Classify the preparation.
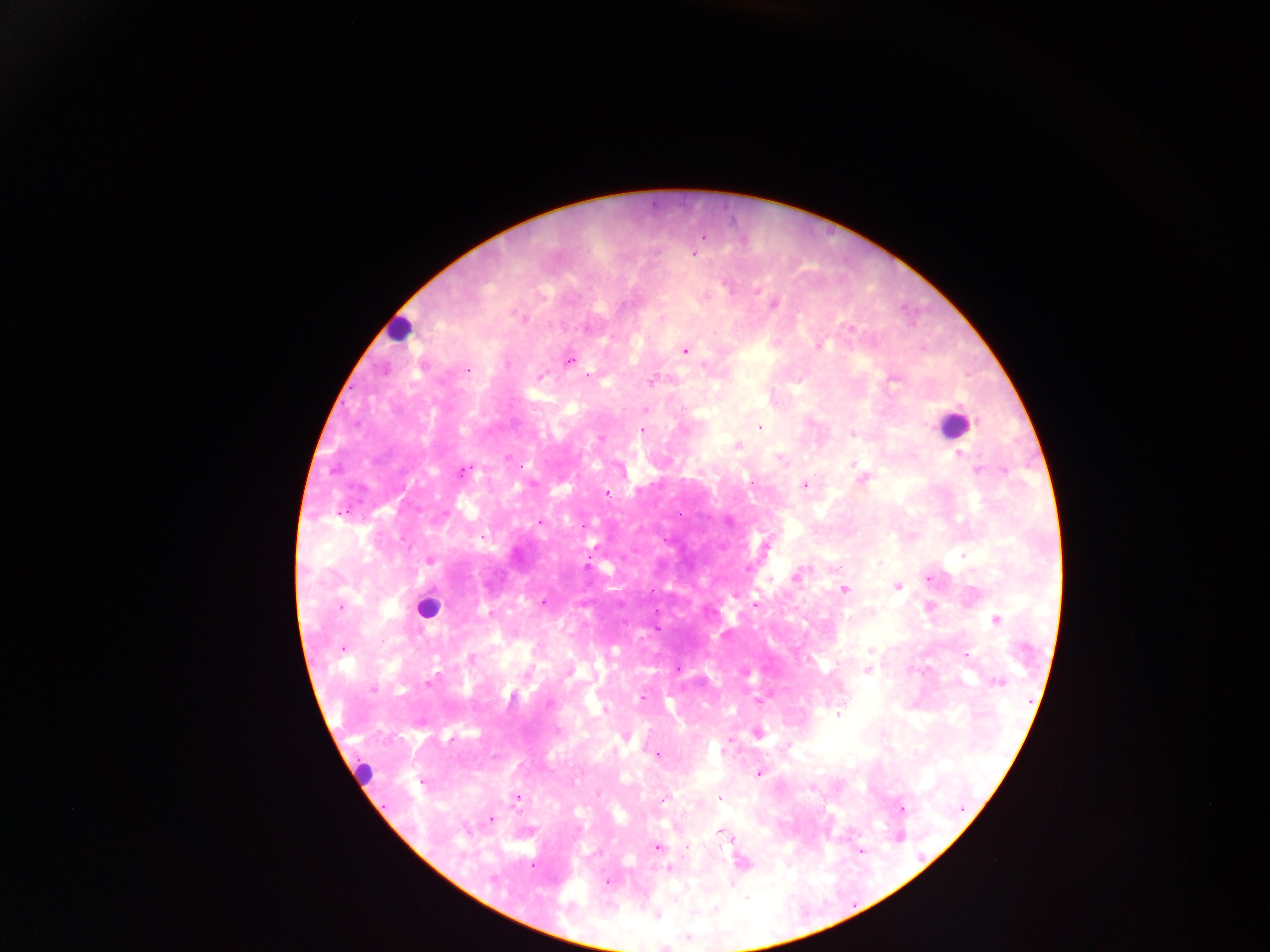
Thick blood smear.

image size = 1270×952 pixels
leukocyte locations = approximate centers as (x, y) in pixels: (398, 331), (953, 422), (428, 608)
country = Ghana
field of view = single
Plasmodium parasite locations = approximate centers as (x, y) in pixels: (702, 236), (693, 252), (725, 284), (757, 290), (706, 295), (773, 305), (512, 313), (854, 325), (586, 327), (849, 328), (820, 345), (827, 345), (686, 351), (569, 360), (467, 369), (590, 375), (541, 376), (894, 380), (651, 383), (646, 409), (758, 425), (641, 431), (852, 434), (599, 438), (737, 447), (961, 452), (506, 457), (852, 462), (978, 469), (463, 472), (864, 480), (803, 485), (607, 495), (541, 522), (763, 545), (430, 560), (748, 565), (586, 566), (796, 576), (898, 587), (845, 590), (543, 600), (756, 605), (994, 620), (345, 647), (342, 650), (871, 650), (472, 656), (678, 669), (741, 670), (869, 670), (745, 673), (430, 682), (373, 689), (642, 698), (758, 699), (552, 704), (835, 716), (759, 734), (655, 756), (366, 770), (757, 774), (418, 781), (810, 788), (516, 797), (718, 797), (663, 798), (901, 809), (490, 818), (720, 830), (728, 834), (658, 848), (670, 870), (607, 881), (657, 917)
capture = mobile-phone photograph through a microscope